Report the malaria status of this cell.
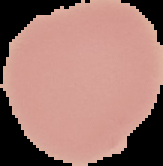
Uninfected.

image_size: 163×166 pixels
image_type: segmented cell region on a black background
preparation: thin blood film